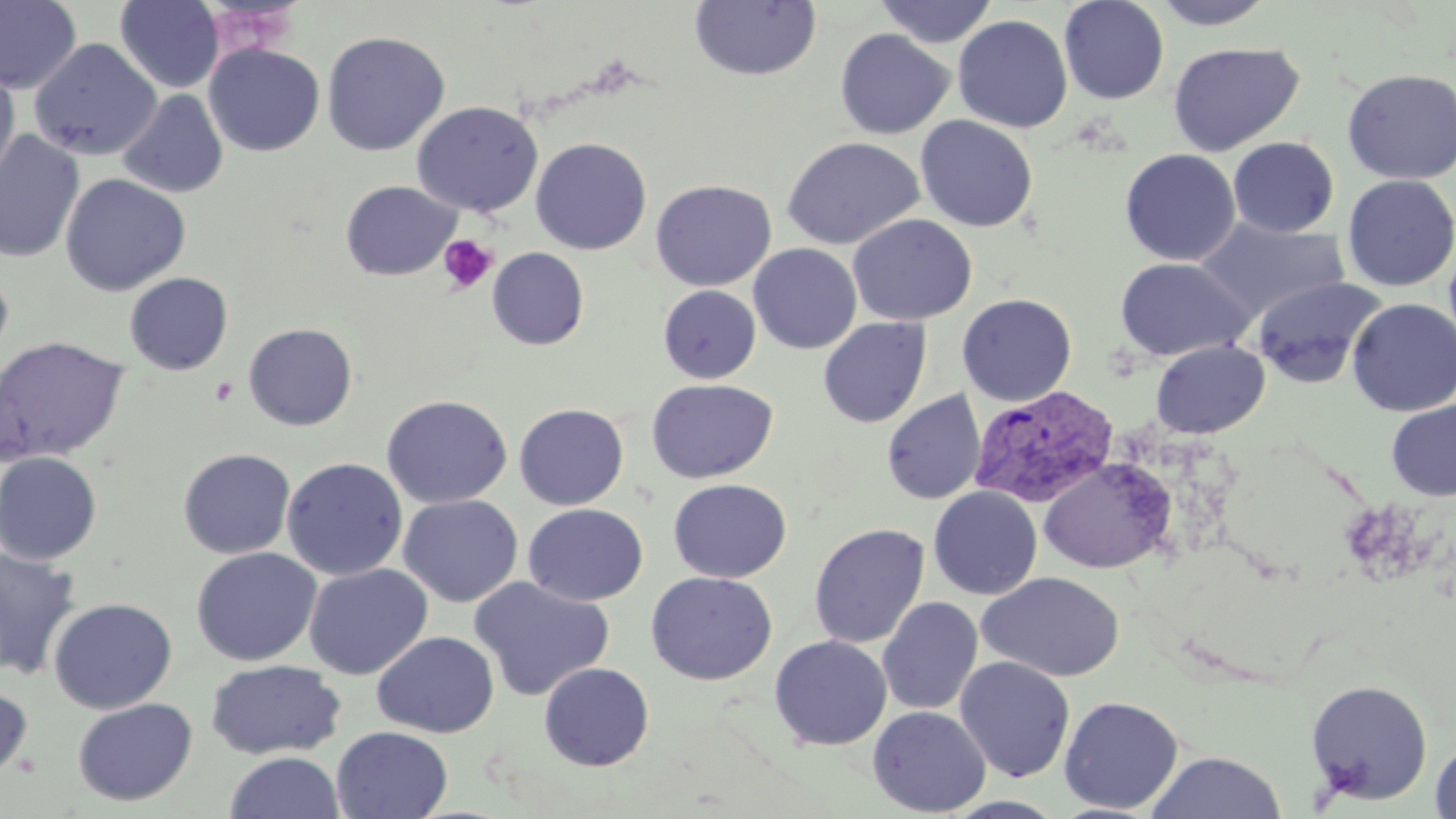
{
  "slide_level_diagnosis": "Plasmodium vivax",
  "stain": "May-Grünwald-Giemsa",
  "field_of_view": "single",
  "modality": "optical microscopy",
  "uninfected_red_blood_cell_locations": "approximate bounding boxes as [x1, y1, x2, y2] in pixels: [0, 0, 82, 95], [689, 0, 821, 82], [873, 0, 999, 48], [1058, 0, 1170, 105], [1150, 0, 1278, 30], [114, 1, 224, 93], [952, 14, 1073, 133], [835, 28, 956, 140], [320, 30, 450, 156], [28, 38, 161, 161], [203, 42, 325, 157], [1168, 42, 1303, 156], [0, 61, 20, 193], [1341, 67, 1456, 184], [116, 88, 228, 199], [410, 101, 543, 217], [915, 115, 1038, 232], [0, 129, 85, 263], [782, 136, 925, 250], [1228, 136, 1339, 238], [530, 137, 652, 255], [1119, 149, 1241, 267], [60, 173, 191, 296], [1341, 174, 1456, 291], [649, 179, 776, 291], [340, 180, 461, 281], [847, 214, 977, 326], [1197, 217, 1350, 321], [1444, 238, 1456, 357], [748, 243, 862, 354], [487, 247, 589, 350], [1114, 257, 1253, 362], [0, 262, 14, 369], [124, 272, 233, 375], [1249, 276, 1388, 389], [658, 285, 761, 383], [957, 293, 1077, 406], [1347, 298, 1456, 417], [817, 316, 931, 429], [243, 322, 358, 431], [0, 335, 130, 463], [1150, 340, 1269, 438], [645, 378, 778, 483], [881, 389, 986, 505], [381, 394, 513, 509], [1386, 399, 1456, 501], [514, 403, 629, 510], [177, 447, 296, 559], [0, 451, 102, 565], [281, 457, 408, 581], [1038, 457, 1175, 573], [668, 478, 791, 583], [928, 486, 1043, 600], [397, 494, 523, 607], [523, 503, 648, 605], [809, 523, 930, 649], [190, 546, 322, 666], [0, 548, 82, 679], [303, 563, 433, 680], [645, 571, 777, 685], [977, 571, 1124, 682], [468, 576, 615, 702], [878, 596, 983, 715], [48, 597, 178, 714], [372, 631, 499, 738], [769, 636, 892, 751], [954, 656, 1075, 782], [205, 659, 346, 759], [538, 662, 655, 771], [1305, 679, 1433, 805], [0, 680, 33, 784], [1059, 696, 1184, 814], [72, 697, 198, 806], [867, 706, 991, 817], [331, 726, 453, 819], [1429, 737, 1456, 819], [1145, 750, 1287, 818], [223, 751, 346, 819], [941, 795, 1069, 818]",
  "image_size": "1456×819 pixels",
  "platelet_locations": "approximate bounding boxes as [x1, y1, x2, y2] in pixels: [437, 234, 498, 295]",
  "preparation": "thin blood film",
  "plasmodium_vivax_infected_red_blood_cell_locations": "approximate bounding boxes as [x1, y1, x2, y2] in pixels: [968, 386, 1119, 509]",
  "magnification": "1000x"
}